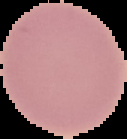

The area outside the segmented cell region is set to black. Malaria status: uninfected. From a thin blood film. Image is 127×139 pixels.